Assess this cell for malaria.
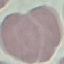
It is uninfected.

Thin blood smear. Photographed with a smartphone camera at the microscope eyepiece. Automatically extracted cell patch, resized to 64 × 64 pixels. Giemsa-stained preparation.